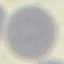

{
  "malaria_status": "uninfected",
  "capture": "smartphone through the microscope eyepiece",
  "stain": "Giemsa",
  "preparation": "thin blood smear",
  "image_type": "cell patch, automatically extracted from a larger field of view and resized to 64 × 64 pixels"
}